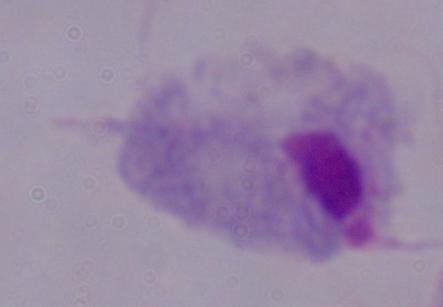

Summary:
  - Modality: photomicrograph
  - Magnification: 1000x
  - Identification: trichomonad